Classify this cell by malaria status.
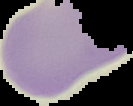
Uninfected.

preparation: thin blood smear
image_size: 133×106 pixels
image_type: segmented cell region on a black background